Identify the parasite.
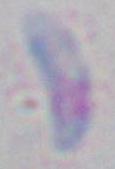

Toxoplasma gondii.

modality = micrograph
magnification = 1000x